State which parasite is depicted.
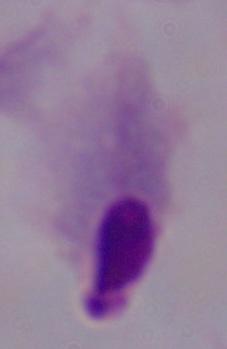
A trichomonad.

Summary:
  - Modality: micrograph
  - Magnification: 1000x